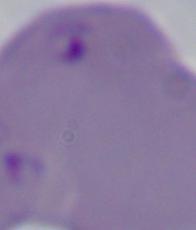

1000x magnification. Photomicrograph. A Babesia parasite is shown.